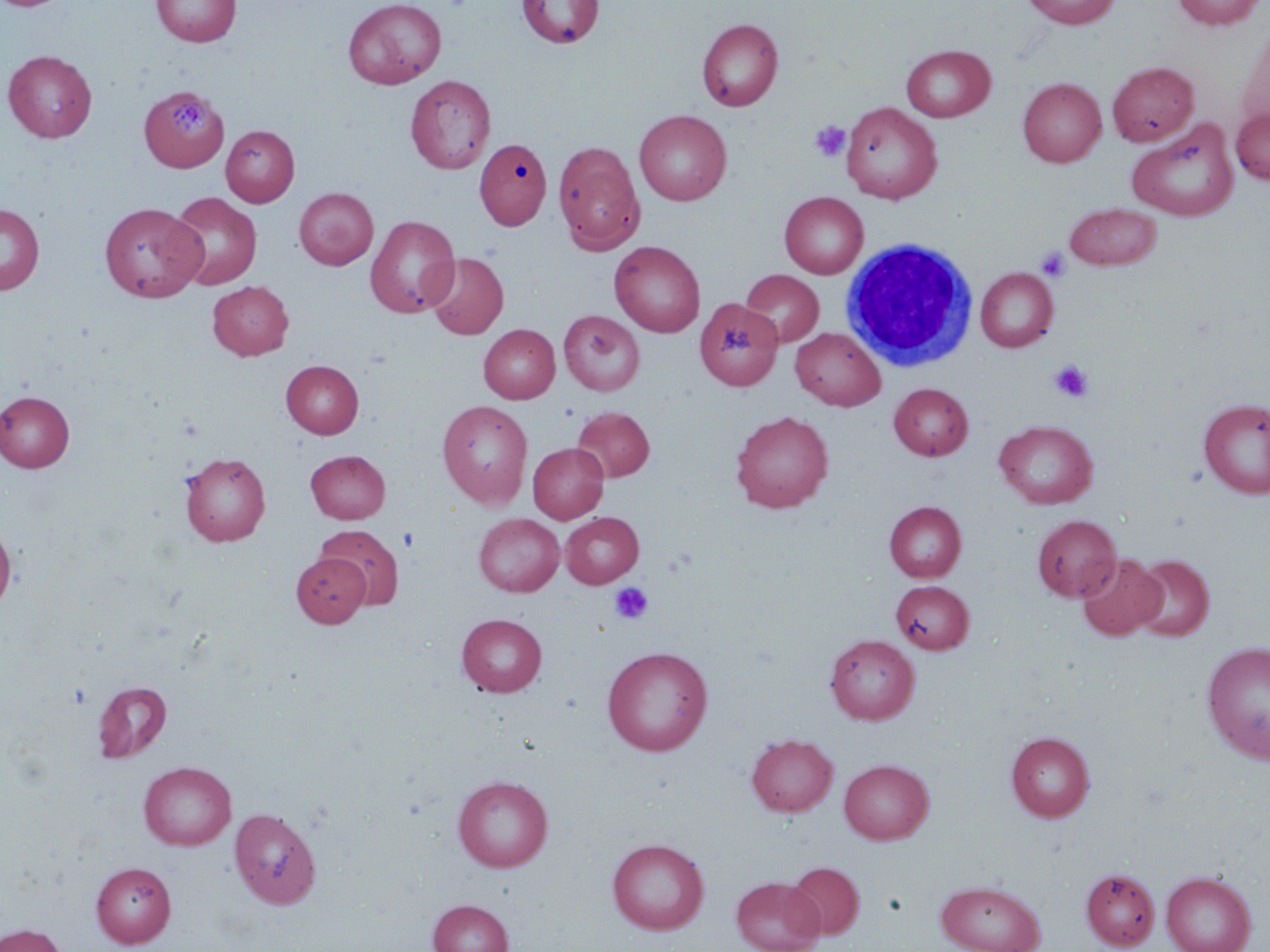
Summary:
  - Coordinate format: approximate bounding boxes as named x1/y1/x2/y2 corners in pixels
  - Uninfected red blood cell locations: (x1=0, y1=0, x2=71, y2=11), (x1=151, y1=0, x2=242, y2=47), (x1=342, y1=0, x2=447, y2=89), (x1=516, y1=0, x2=604, y2=49), (x1=1022, y1=0, x2=1121, y2=29), (x1=1173, y1=0, x2=1266, y2=29), (x1=696, y1=18, x2=783, y2=111), (x1=1236, y1=25, x2=1270, y2=133), (x1=902, y1=44, x2=996, y2=122), (x1=3, y1=50, x2=97, y2=142), (x1=1107, y1=61, x2=1198, y2=146), (x1=1018, y1=74, x2=1199, y2=159), (x1=406, y1=75, x2=496, y2=174), (x1=1018, y1=77, x2=1106, y2=167), (x1=139, y1=86, x2=228, y2=171), (x1=841, y1=102, x2=942, y2=204), (x1=1231, y1=108, x2=1270, y2=185), (x1=634, y1=110, x2=732, y2=205), (x1=1127, y1=117, x2=1239, y2=222), (x1=221, y1=125, x2=299, y2=207), (x1=474, y1=138, x2=551, y2=230), (x1=553, y1=141, x2=645, y2=255), (x1=294, y1=188, x2=378, y2=269), (x1=780, y1=191, x2=868, y2=279), (x1=167, y1=192, x2=262, y2=290), (x1=100, y1=202, x2=206, y2=302), (x1=1064, y1=202, x2=1162, y2=271), (x1=0, y1=203, x2=44, y2=294), (x1=365, y1=214, x2=461, y2=318), (x1=609, y1=240, x2=705, y2=337), (x1=426, y1=252, x2=508, y2=339), (x1=976, y1=267, x2=1058, y2=352), (x1=741, y1=269, x2=824, y2=347), (x1=207, y1=281, x2=293, y2=360), (x1=694, y1=297, x2=783, y2=390), (x1=558, y1=310, x2=645, y2=395), (x1=479, y1=324, x2=560, y2=403), (x1=790, y1=327, x2=886, y2=410), (x1=281, y1=360, x2=364, y2=438), (x1=889, y1=383, x2=973, y2=460), (x1=0, y1=390, x2=75, y2=472), (x1=1198, y1=398, x2=1270, y2=498), (x1=438, y1=400, x2=533, y2=509), (x1=572, y1=406, x2=654, y2=482), (x1=731, y1=411, x2=833, y2=512), (x1=994, y1=419, x2=1098, y2=509), (x1=528, y1=442, x2=608, y2=523), (x1=305, y1=450, x2=390, y2=523), (x1=180, y1=453, x2=270, y2=545), (x1=884, y1=501, x2=966, y2=582), (x1=560, y1=512, x2=644, y2=587), (x1=473, y1=513, x2=565, y2=596), (x1=1032, y1=515, x2=1121, y2=601), (x1=0, y1=523, x2=16, y2=614), (x1=316, y1=524, x2=404, y2=609), (x1=291, y1=552, x2=370, y2=627), (x1=1077, y1=553, x2=1166, y2=641), (x1=1131, y1=554, x2=1214, y2=641), (x1=891, y1=580, x2=973, y2=654), (x1=456, y1=613, x2=548, y2=697), (x1=825, y1=634, x2=920, y2=724), (x1=1201, y1=640, x2=1270, y2=764), (x1=602, y1=646, x2=713, y2=756), (x1=93, y1=681, x2=172, y2=762), (x1=1006, y1=731, x2=1094, y2=821), (x1=746, y1=734, x2=838, y2=816), (x1=839, y1=759, x2=934, y2=844), (x1=139, y1=761, x2=236, y2=850), (x1=453, y1=775, x2=553, y2=872), (x1=229, y1=807, x2=321, y2=908), (x1=607, y1=838, x2=708, y2=934), (x1=786, y1=861, x2=865, y2=939), (x1=91, y1=862, x2=176, y2=947), (x1=1081, y1=868, x2=1160, y2=951), (x1=1161, y1=871, x2=1256, y2=952), (x1=731, y1=876, x2=825, y2=952), (x1=936, y1=880, x2=1046, y2=952), (x1=428, y1=899, x2=513, y2=952), (x1=0, y1=924, x2=66, y2=952)
  - White blood cell locations: (x1=841, y1=237, x2=978, y2=372)
  - Platelet locations: (x1=170, y1=99, x2=209, y2=139), (x1=810, y1=121, x2=851, y2=162), (x1=1035, y1=246, x2=1071, y2=281), (x1=1049, y1=360, x2=1094, y2=402), (x1=609, y1=582, x2=654, y2=624)
  - Slide-level diagnosis: no evidence of blood parasites
  - Image size: 1270×952 pixels
  - Modality: light microscopy
  - Stain: May-Grünwald-Giemsa
  - Field of view: single
  - Preparation: thin blood film
  - Magnification: 1000x